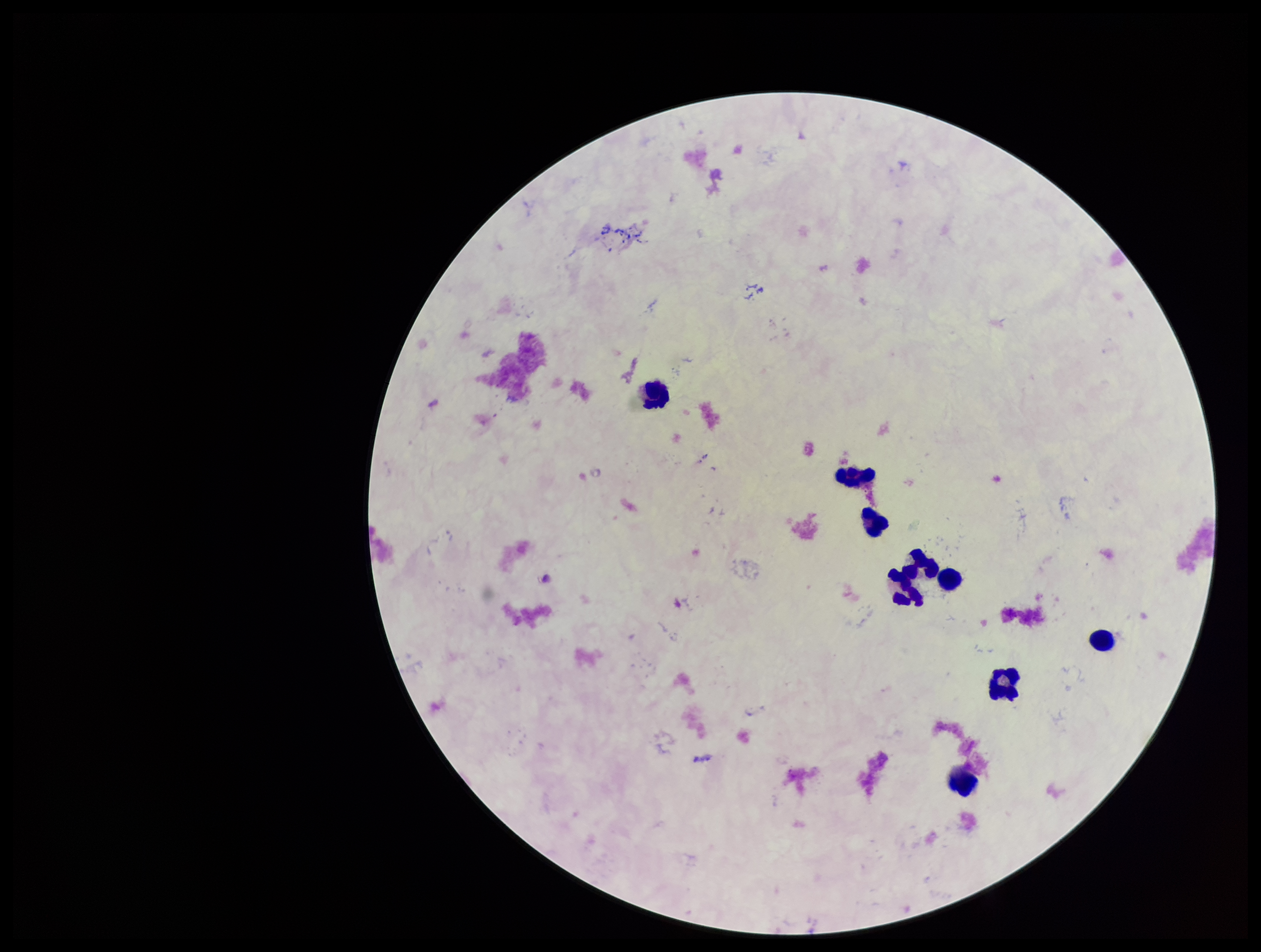
stain = Giemsa
image size = 1261×952 pixels
preparation = thick
field of view = single
capture = smartphone photograph through the microscope eyepiece
Plasmodium parasites = none identified
leukocyte count = 9
parasite count = 0
patient malaria status = negative